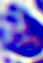

Photomicrograph. Captured at 400x magnification. A leukocyte is shown.